Assess this cell for malaria.
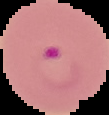

Parasitized.

{
  "image_size": "109×115 pixels",
  "preparation": "thin blood smear",
  "image_type": "segmented cell region on a black background"
}